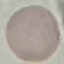
Summary:
  - Result: negative for malaria parasites
  - Stain: Giemsa
  - Preparation: thin blood smear
  - Image type: automatically extracted cell patch, resized to 64 × 64 pixels
  - Capture: smartphone camera at the microscope eyepiece